Locate every Plasmodium falciparum-infected red blood cell.
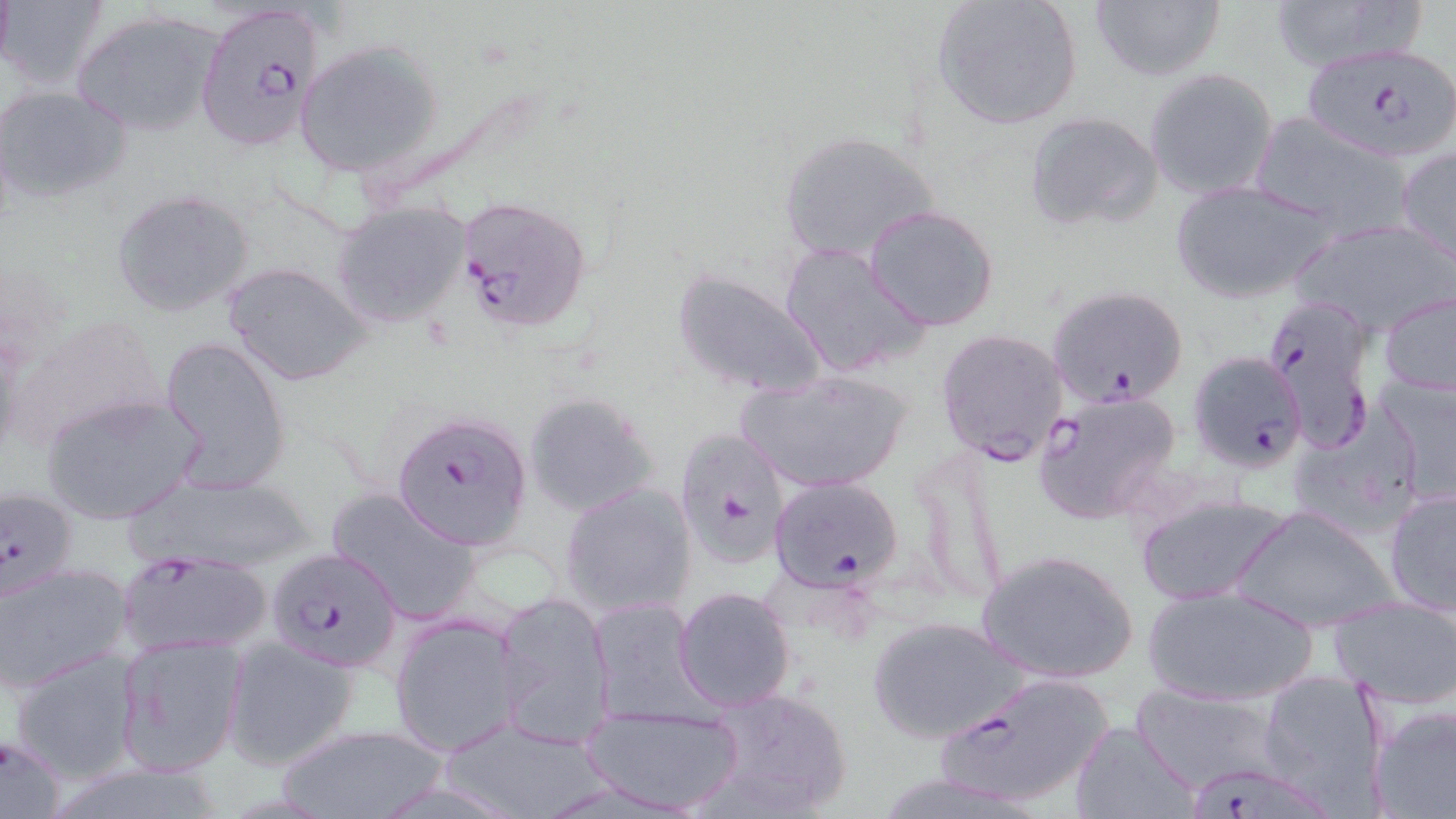
Approximate bounding boxes as [x1, y1, x2, y2] in pixels.
Plasmodium falciparum-infected red blood cells: [192, 1, 325, 155], [1304, 43, 1456, 162], [456, 196, 592, 334], [1047, 284, 1190, 409], [1262, 293, 1378, 455], [935, 327, 1072, 465], [1189, 350, 1309, 472], [1033, 391, 1184, 522], [393, 412, 533, 550], [674, 424, 793, 567], [767, 475, 904, 592], [0, 486, 79, 604], [265, 546, 404, 672], [115, 549, 273, 658], [932, 670, 1113, 811], [0, 732, 66, 819], [1185, 762, 1336, 819].

Uninfected red blood cell locations: [1, 0, 108, 91], [931, 0, 1083, 130], [1263, 0, 1422, 71], [1089, 1, 1224, 82], [70, 9, 225, 139], [294, 38, 447, 180], [1144, 67, 1278, 200], [359, 77, 557, 215], [1, 84, 131, 205], [1023, 110, 1165, 232], [1252, 114, 1417, 240], [776, 129, 941, 267], [1397, 145, 1456, 265], [1170, 180, 1335, 305], [109, 188, 256, 320], [330, 201, 471, 329], [864, 204, 1000, 331], [1291, 217, 1456, 336], [778, 241, 931, 379], [224, 262, 372, 387], [671, 267, 830, 400], [1379, 291, 1456, 399], [12, 314, 169, 455], [159, 337, 290, 491], [738, 369, 912, 495], [1371, 374, 1456, 506], [40, 391, 203, 524], [522, 391, 660, 518], [1293, 406, 1422, 538], [135, 473, 319, 572], [560, 482, 697, 618], [324, 486, 485, 624], [1384, 487, 1455, 617], [1134, 494, 1291, 605], [1359, 495, 1454, 705], [1232, 504, 1398, 633], [976, 548, 1139, 683], [1, 560, 131, 693], [1141, 584, 1317, 708], [673, 586, 796, 712], [492, 590, 617, 748], [588, 597, 705, 723], [1329, 598, 1456, 709], [390, 614, 522, 756], [868, 615, 1026, 744], [113, 635, 246, 776], [224, 638, 361, 771], [8, 649, 143, 785], [1257, 669, 1393, 813], [1132, 684, 1285, 794], [704, 685, 853, 816], [580, 703, 745, 814], [1368, 705, 1456, 818], [437, 714, 609, 819], [1069, 720, 1201, 818], [267, 721, 452, 819]. Slide-level diagnosis: Plasmodium falciparum. Thin blood smear. Image is 1456×819 pixels. May-Grünwald-Giemsa-stained preparation. Single field of view. Light microscopy. 1000x magnification.